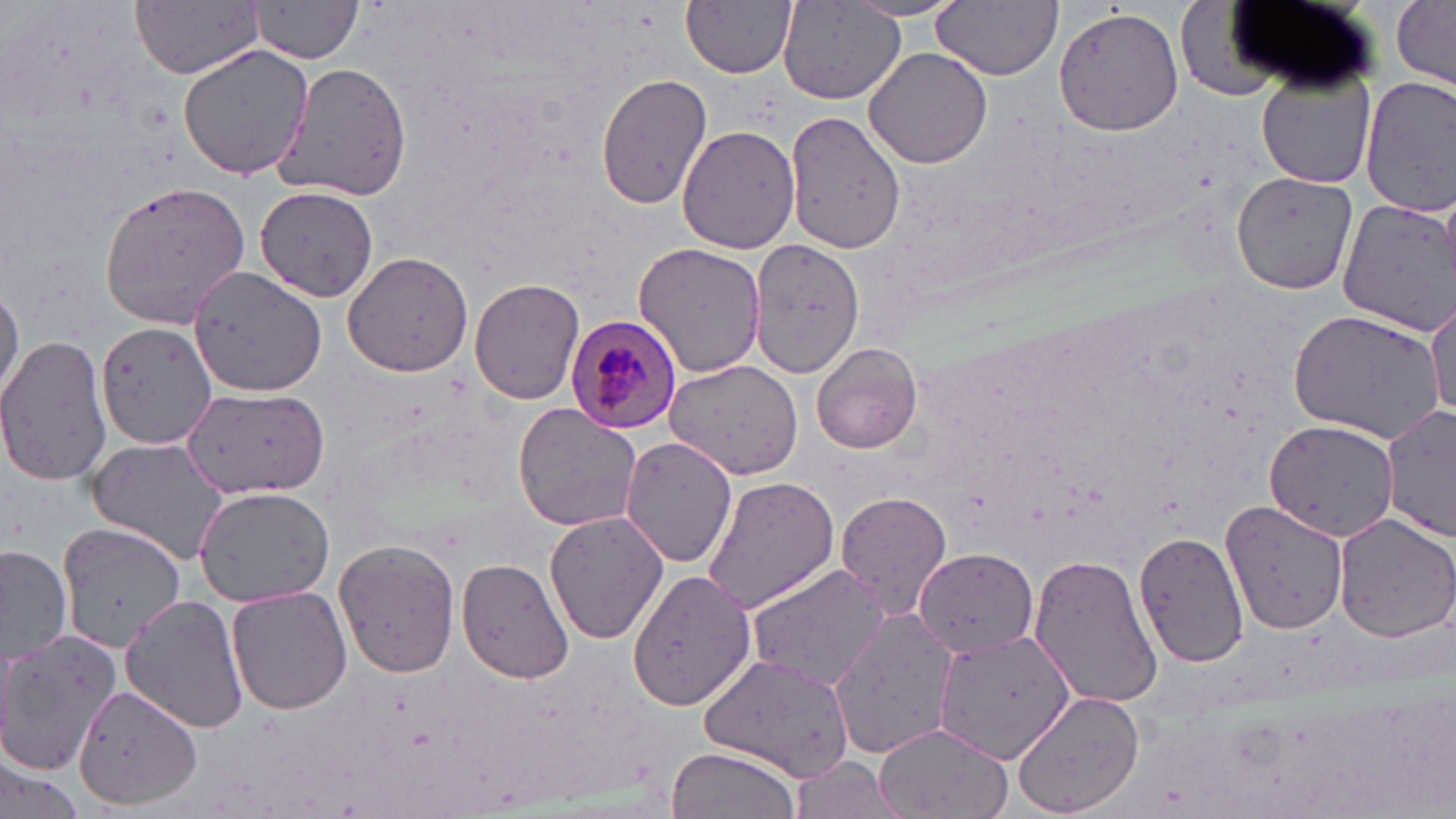

slide_level_diagnosis: Plasmodium malariae
uninfected_red_blood_cell_locations: 'approximate bounding boxes as named x1/y1/x2/y2 corners in pixels: (x1=132, y1=0, x2=265, y2=78), (x1=683, y1=0, x2=798, y2=77), (x1=931, y1=0, x2=1063, y2=80), (x1=250, y1=1, x2=361, y2=64), (x1=776, y1=1, x2=905, y2=106), (x1=1392, y1=2, x2=1454, y2=88), (x1=1054, y1=5, x2=1184, y2=136), (x1=177, y1=43, x2=319, y2=180), (x1=865, y1=46, x2=994, y2=169), (x1=275, y1=63, x2=411, y2=200), (x1=1257, y1=64, x2=1378, y2=187), (x1=596, y1=72, x2=712, y2=212), (x1=1360, y1=75, x2=1456, y2=215), (x1=785, y1=109, x2=904, y2=254), (x1=677, y1=125, x2=800, y2=254), (x1=1231, y1=172, x2=1360, y2=294), (x1=98, y1=182, x2=252, y2=331), (x1=253, y1=185, x2=379, y2=300), (x1=1338, y1=198, x2=1454, y2=332), (x1=747, y1=240, x2=870, y2=379), (x1=633, y1=242, x2=771, y2=378), (x1=342, y1=250, x2=475, y2=377), (x1=187, y1=264, x2=329, y2=397), (x1=469, y1=277, x2=585, y2=405), (x1=0, y1=281, x2=23, y2=412), (x1=1427, y1=296, x2=1456, y2=416), (x1=1286, y1=308, x2=1443, y2=441), (x1=97, y1=320, x2=218, y2=450), (x1=0, y1=336, x2=112, y2=487), (x1=811, y1=343, x2=923, y2=454), (x1=666, y1=357, x2=804, y2=480), (x1=178, y1=388, x2=329, y2=497), (x1=512, y1=402, x2=643, y2=533), (x1=1382, y1=405, x2=1456, y2=543), (x1=1267, y1=418, x2=1397, y2=539), (x1=620, y1=435, x2=737, y2=569), (x1=85, y1=437, x2=233, y2=564), (x1=702, y1=475, x2=842, y2=614), (x1=193, y1=483, x2=334, y2=608), (x1=836, y1=491, x2=953, y2=618), (x1=1223, y1=501, x2=1348, y2=635), (x1=544, y1=510, x2=668, y2=645), (x1=1332, y1=513, x2=1456, y2=642), (x1=57, y1=523, x2=186, y2=650), (x1=1137, y1=530, x2=1249, y2=668), (x1=334, y1=536, x2=460, y2=679), (x1=0, y1=543, x2=72, y2=670), (x1=915, y1=547, x2=1039, y2=656), (x1=1028, y1=553, x2=1166, y2=710), (x1=456, y1=557, x2=573, y2=684), (x1=745, y1=563, x2=889, y2=688), (x1=628, y1=567, x2=756, y2=712), (x1=227, y1=585, x2=352, y2=716), (x1=120, y1=595, x2=250, y2=734), (x1=830, y1=609, x2=957, y2=759), (x1=935, y1=626, x2=1081, y2=763), (x1=0, y1=629, x2=121, y2=772), (x1=700, y1=654, x2=856, y2=780), (x1=74, y1=686, x2=201, y2=808), (x1=1012, y1=687, x2=1145, y2=819), (x1=871, y1=724, x2=1013, y2=819), (x1=664, y1=746, x2=802, y2=819), (x1=789, y1=755, x2=902, y2=819), (x1=0, y1=757, x2=86, y2=819)'
image_size: 1456×819 pixels
modality: light microscopy
field_of_view: one of a larger specimen
plasmodium_malariae_infected_red_blood_cell_locations: 'approximate bounding boxes as named x1/y1/x2/y2 corners in pixels: (x1=565, y1=312, x2=684, y2=432)'
magnification: 1000x
preparation: thin blood smear
stain: May-Grünwald-Giemsa